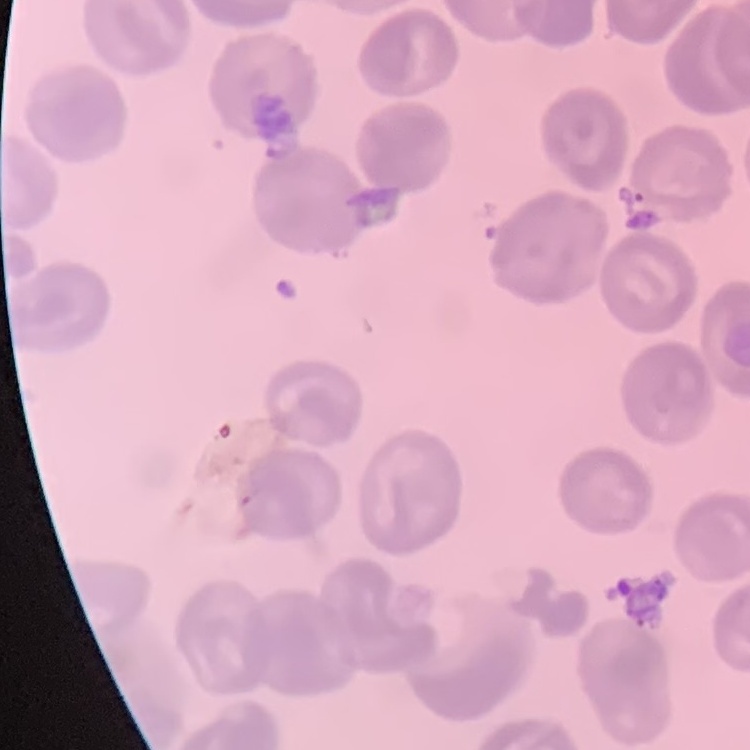

Summary:
  - Erythrocyte morphology: no rouleaux formation
  - Preparation: thin blood film
  - Image type: square crop of a larger photomicrograph
  - Stain: Field's or Giemsa